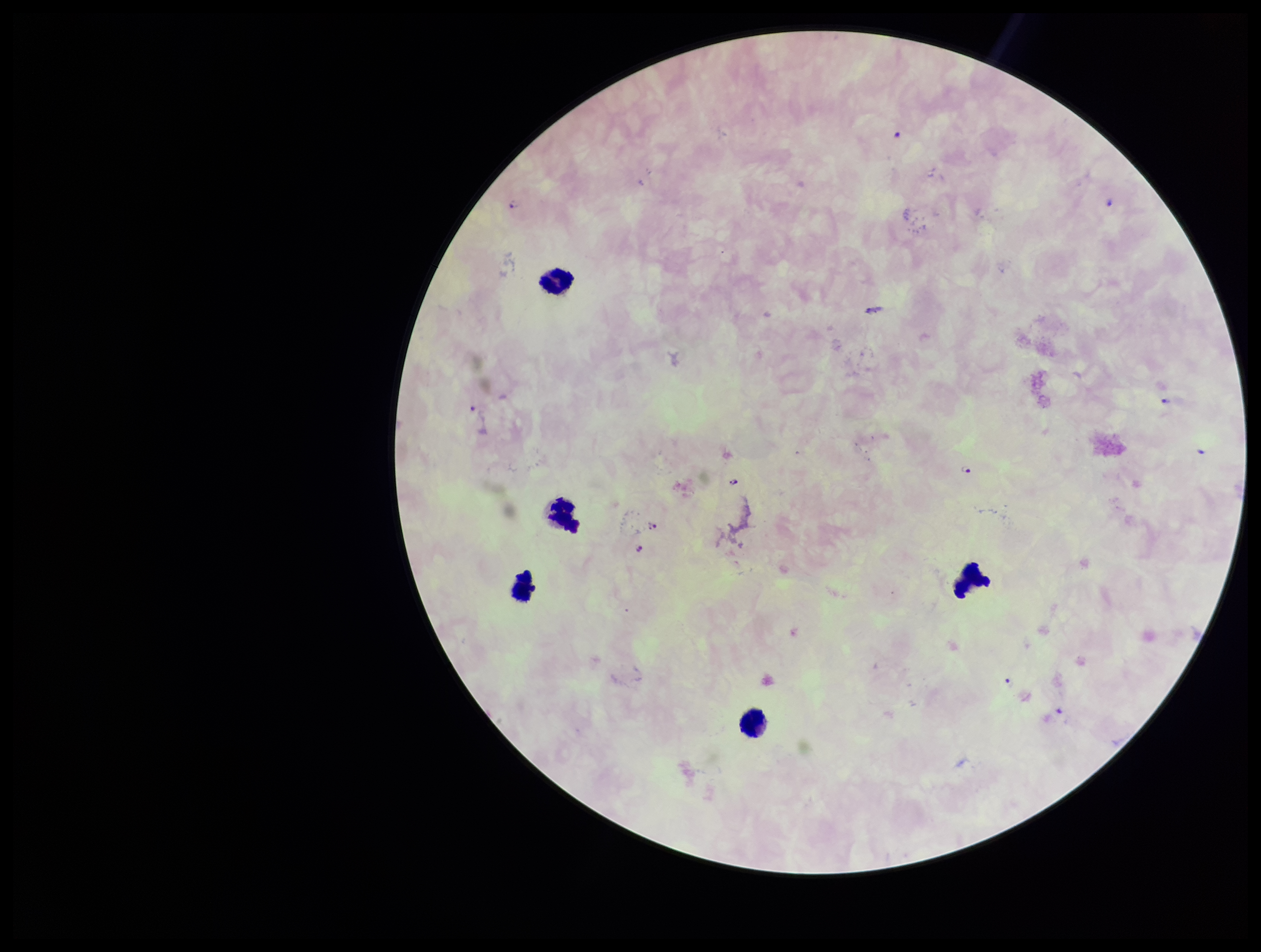
Parasite count: 10. Image is 1261×952 pixels. Plasmodium parasites: identified. One field from this slide. Stained with Giemsa. Smartphone photograph taken through the eyepiece of a microscope. Species reported for this patient: Plasmodium falciparum. Leukocyte count: 5. Preparation: thick. Patient malaria status: positive.